Give the preparation type.
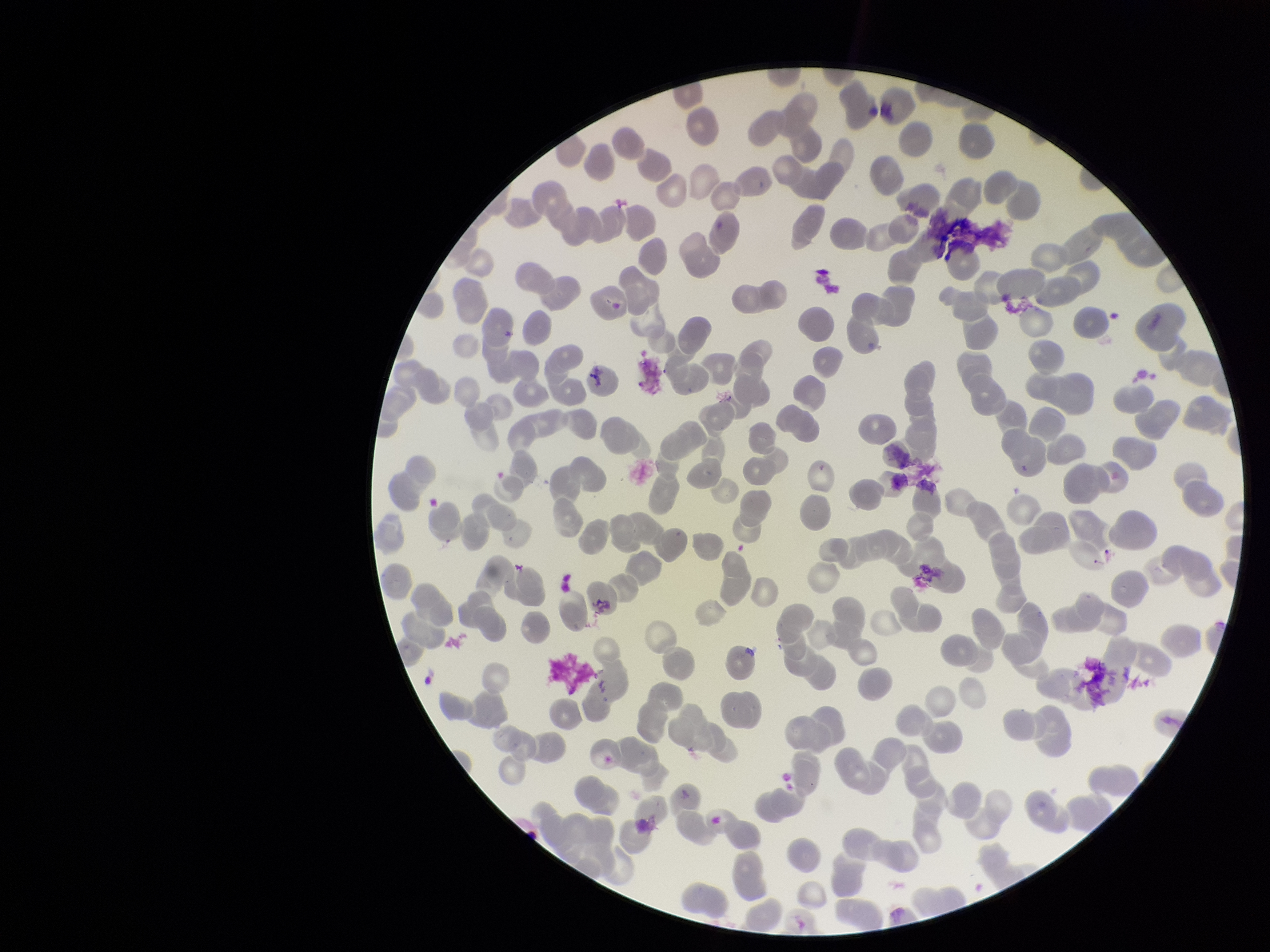
A thin smear.

{
  "parasitized_red_blood_cells": "none identified",
  "parasitized_red_blood_cell_count": 0,
  "red_blood_cell_count": 236,
  "capture": "smartphone photograph through the microscope eyepiece",
  "stain": "Giemsa",
  "patient_malaria_status": "negative",
  "image_size": "1270×952 pixels",
  "field_of_view": "single"
}